Assess the morphology of the erythrocytes.
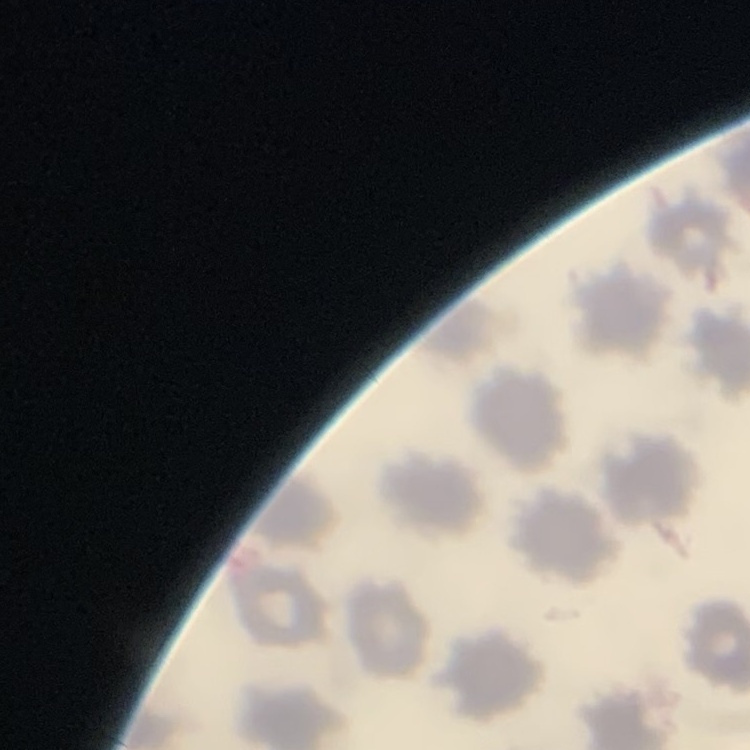

They show no rouleaux formation.

Summary:
  - Image type: one tile cut from a larger photomicrograph
  - Stain: Field's or Giemsa
  - Preparation: thin blood smear